Describe the morphology of the red blood cells.
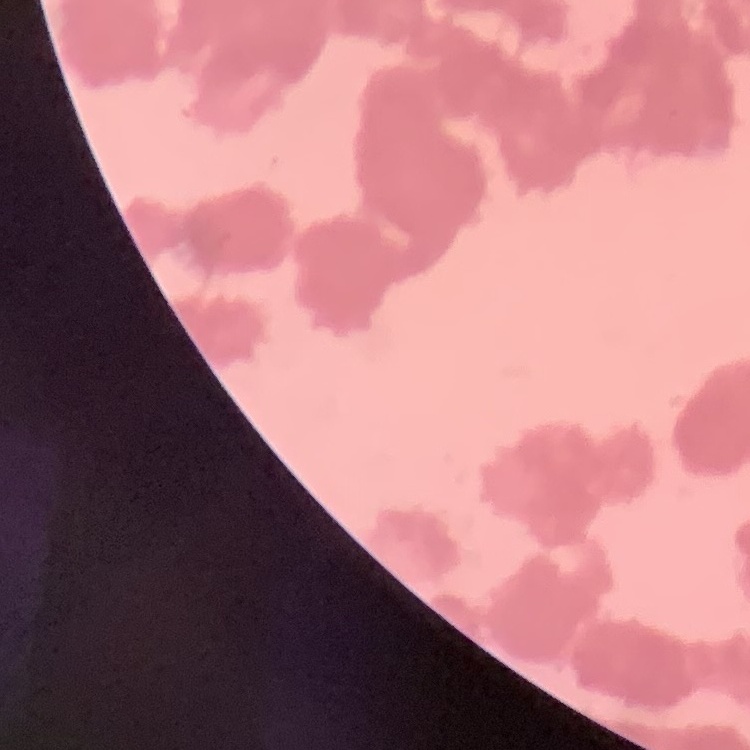
They show rouleaux formation.

Summary:
  - Stain: Field's or Giemsa
  - Image type: square crop of a larger photomicrograph
  - Preparation: thin blood film